State the blood parasite species.
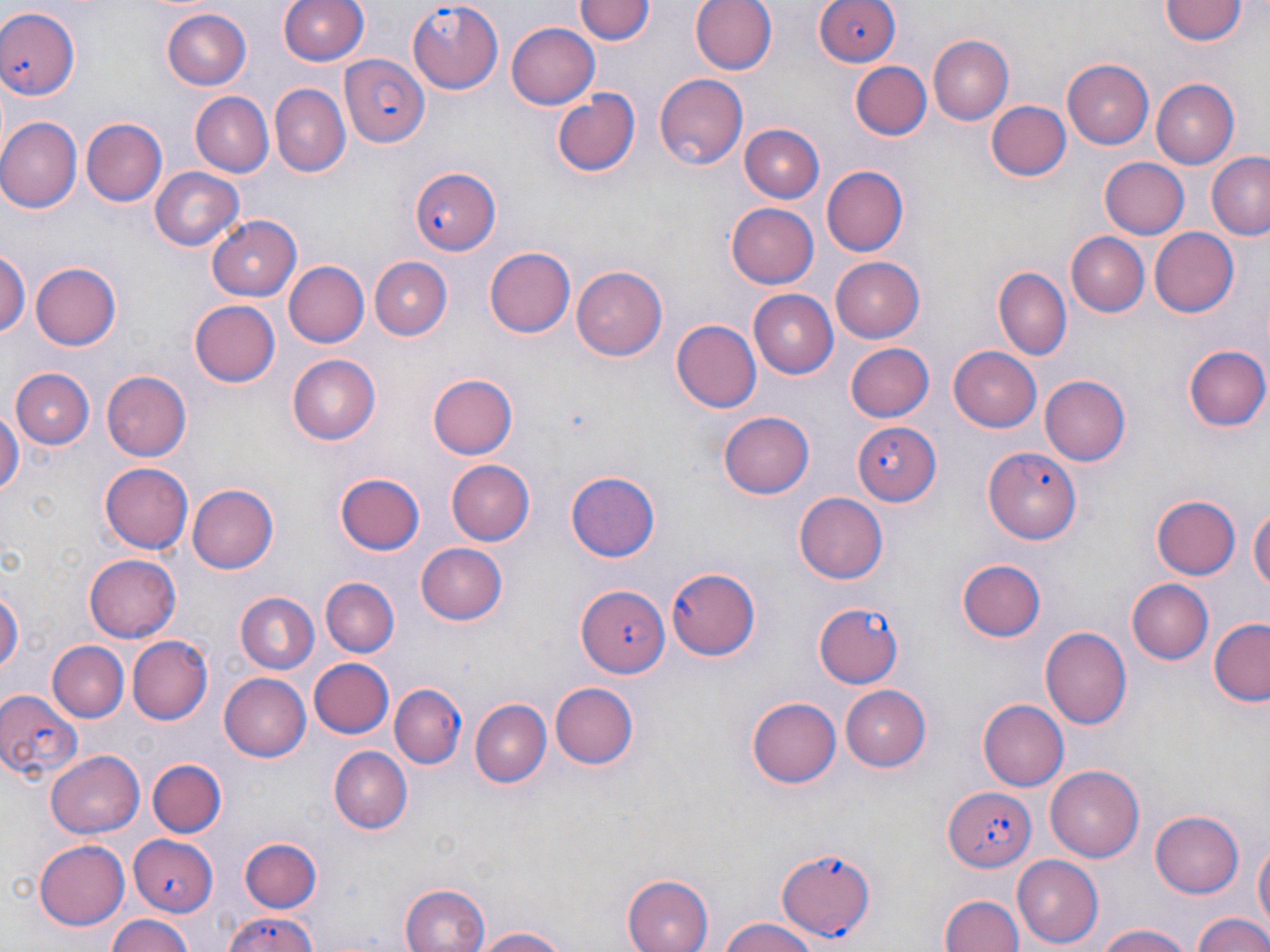

Plasmodium falciparum.

Summary:
  - Coordinate format: approximate bounding boxes as (x1, y1, x2, y2) in pixels
  - Uninfected red blood cell locations: (279, 0, 370, 67), (577, 0, 652, 47), (692, 0, 778, 76), (1160, 1, 1246, 47), (160, 10, 251, 90), (507, 24, 599, 108), (928, 35, 1016, 125), (1061, 57, 1153, 149), (851, 62, 930, 140), (655, 74, 748, 170), (1152, 79, 1240, 167), (268, 85, 350, 177), (552, 90, 642, 179), (189, 91, 273, 176), (984, 100, 1070, 183), (0, 118, 81, 214), (82, 118, 167, 206), (742, 125, 826, 203), (1207, 153, 1270, 241), (1102, 157, 1191, 238), (821, 165, 908, 257), (151, 167, 243, 250), (725, 201, 817, 288), (208, 214, 301, 298), (1150, 227, 1240, 317), (1068, 232, 1148, 317), (485, 248, 576, 338), (0, 249, 27, 340), (832, 254, 925, 340), (368, 256, 452, 338), (31, 260, 122, 350), (283, 261, 368, 349), (570, 264, 666, 361), (995, 268, 1071, 358), (749, 289, 837, 378), (189, 300, 281, 388), (671, 321, 761, 412), (845, 343, 933, 423), (1184, 344, 1270, 432), (948, 345, 1041, 432), (288, 355, 381, 445), (11, 367, 95, 449), (101, 368, 193, 463), (1041, 374, 1132, 467), (429, 375, 518, 459), (0, 405, 22, 503), (719, 410, 814, 499), (445, 458, 534, 546), (99, 462, 194, 553), (565, 471, 661, 562), (336, 472, 425, 554), (187, 483, 278, 574), (795, 492, 889, 584), (1151, 495, 1241, 580), (1250, 501, 1269, 604), (415, 543, 509, 625), (85, 553, 180, 641), (958, 558, 1047, 641), (319, 577, 399, 658), (1127, 578, 1213, 664), (0, 579, 22, 685), (234, 590, 319, 672), (1209, 618, 1270, 706), (1040, 624, 1133, 732), (126, 636, 211, 724), (47, 639, 128, 719), (309, 657, 393, 739), (219, 674, 310, 762), (549, 682, 638, 769), (840, 684, 933, 771), (471, 697, 551, 787), (748, 697, 844, 788), (978, 700, 1068, 791), (328, 746, 413, 833), (48, 749, 145, 840), (145, 758, 226, 837), (1047, 764, 1146, 861), (1151, 808, 1244, 896), (240, 837, 321, 914), (1253, 837, 1269, 938), (34, 839, 131, 929), (1011, 854, 1103, 947), (622, 873, 714, 952), (399, 882, 493, 952), (939, 890, 1023, 952), (1191, 912, 1270, 952), (104, 915, 198, 952), (716, 918, 826, 952), (1093, 922, 1199, 952), (469, 926, 575, 951)
  - Plasmodium falciparum-infected red blood cell locations: (407, 0, 503, 91), (811, 0, 898, 70), (0, 5, 82, 101), (340, 54, 430, 148), (407, 166, 502, 255), (851, 420, 942, 508), (984, 449, 1081, 543), (665, 565, 761, 660), (578, 586, 670, 678), (815, 602, 905, 687), (392, 684, 466, 767), (0, 688, 83, 785), (943, 785, 1037, 871), (126, 831, 217, 916), (778, 847, 879, 940), (215, 915, 327, 952)
  - Stain: May-Grünwald-Giemsa
  - Image size: 1270×952 pixels
  - Preparation: thin blood film
  - Modality: light microscopy
  - Magnification: 1000x
  - Field of view: one of a larger specimen